Outline each blood parasite and name the species.
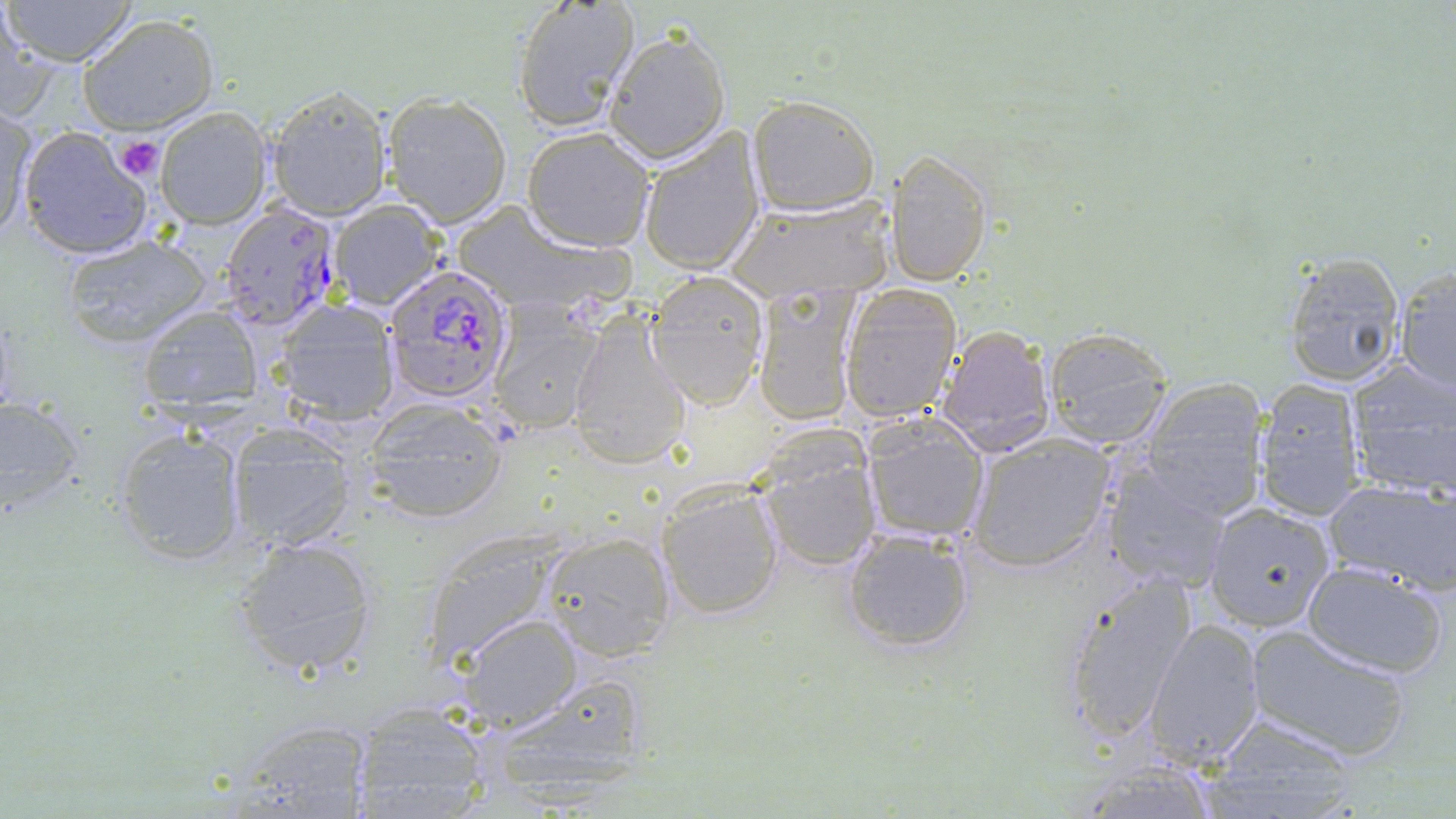
Approximate bounding boxes as (x1, y1, x2, y2) in pixels.
Plasmodium falciparum-infected red blood cells: (220, 203, 343, 331), (382, 263, 514, 402).
No Plasmodium ovale, Plasmodium malariae, Plasmodium vivax, Babesia divergens, or Trypanosoma brucei observed.

Summary:
  - Platelet locations: (113, 135, 165, 182)
  - Uninfected red blood cell locations: (3, 0, 140, 67), (512, 0, 639, 132), (1, 9, 49, 120), (78, 13, 219, 134), (604, 28, 732, 164), (265, 85, 392, 220), (381, 93, 512, 226), (748, 94, 880, 215), (156, 107, 273, 229), (1, 108, 36, 246), (637, 125, 767, 276), (16, 126, 153, 260), (522, 128, 656, 252), (886, 149, 993, 286), (726, 195, 897, 302), (327, 201, 446, 310), (58, 232, 213, 348), (1280, 252, 1406, 388), (1394, 265, 1456, 392), (646, 272, 771, 407), (837, 286, 961, 422), (753, 287, 860, 427), (271, 300, 402, 429), (485, 303, 607, 436), (134, 305, 265, 419), (567, 316, 693, 469), (935, 325, 1058, 455), (1042, 327, 1175, 449), (1343, 357, 1456, 501), (1254, 378, 1366, 521), (1135, 379, 1270, 522), (0, 395, 87, 511), (362, 396, 510, 523), (859, 418, 992, 545), (223, 425, 360, 552), (113, 428, 248, 567), (752, 435, 884, 573), (964, 435, 1115, 572), (1100, 460, 1230, 595), (1324, 476, 1456, 591), (654, 479, 785, 620), (1204, 504, 1335, 632), (842, 527, 976, 653), (538, 529, 678, 661), (425, 531, 569, 665), (231, 535, 379, 675), (1300, 561, 1449, 677), (1057, 572, 1197, 741), (455, 614, 582, 733), (1145, 617, 1265, 768), (1248, 626, 1414, 762), (477, 673, 655, 800), (352, 700, 494, 817), (219, 715, 375, 819), (1208, 715, 1364, 819)
  - Slide-level diagnosis: Plasmodium falciparum
  - Field of view: single
  - Modality: optical microscopy
  - Preparation: thin blood film
  - Stain: May-Grünwald-Giemsa
  - Magnification: 1000x
  - Image size: 1456×819 pixels